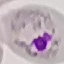

malaria status = parasitized
image type = automatically extracted cell patch, resized to 64 × 64 pixels
capture = smartphone camera at the microscope eyepiece
stain = Giemsa
preparation = thin blood smear